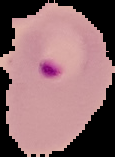 From a thin blood film. Segmented cell region on a black background. Image is 115×157 pixels. Malaria status: parasitized.